Identify the parasite.
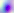

Toxoplasma gondii.

Summary:
  - Modality: micrograph
  - Magnification: 400x